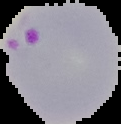
image type = segmented cell region with the area outside set to black
preparation = thin blood film
malaria status = parasitized
image size = 121×124 pixels